Describe the morphology of the erythrocytes.
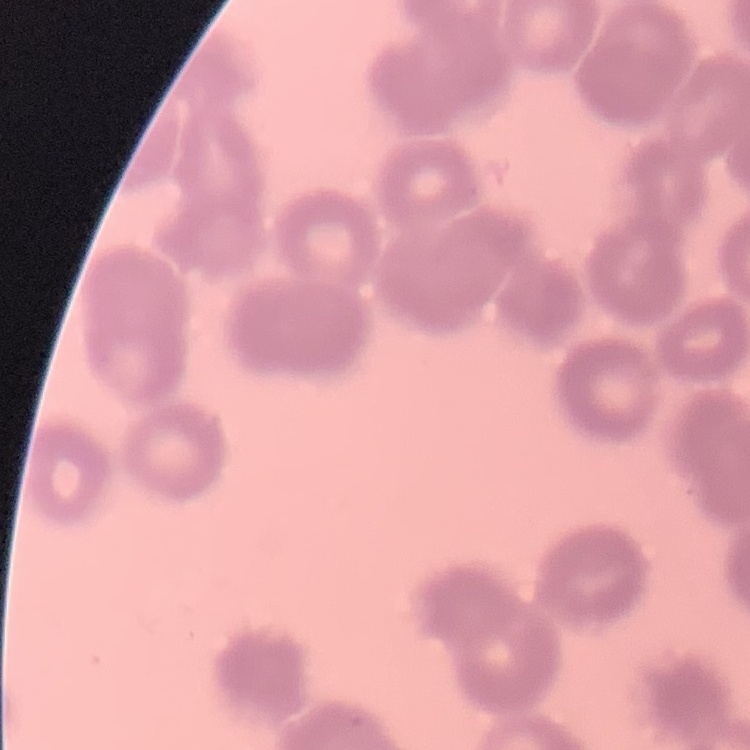
Rouleaux formation.

preparation: thin peripheral smear
image_type: square crop of a larger photomicrograph
stain: Field's or Giemsa